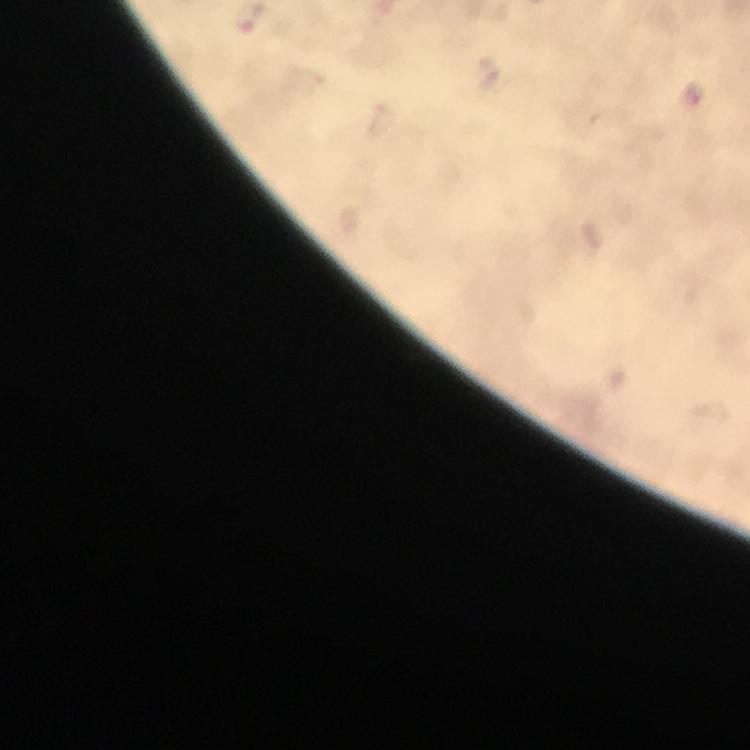

Approximate centers as {x, y} in pixels. Malaria parasite locations: {246, 18}. Giemsa-stained preparation. Immersion oil was used. At 100x magnification. From a diagnostic examination for malaria. Image is 750×750 pixels. A crop from one field of view. Thick blood film. Smartphone photograph taken through a microscope.